Name the blood parasite species.
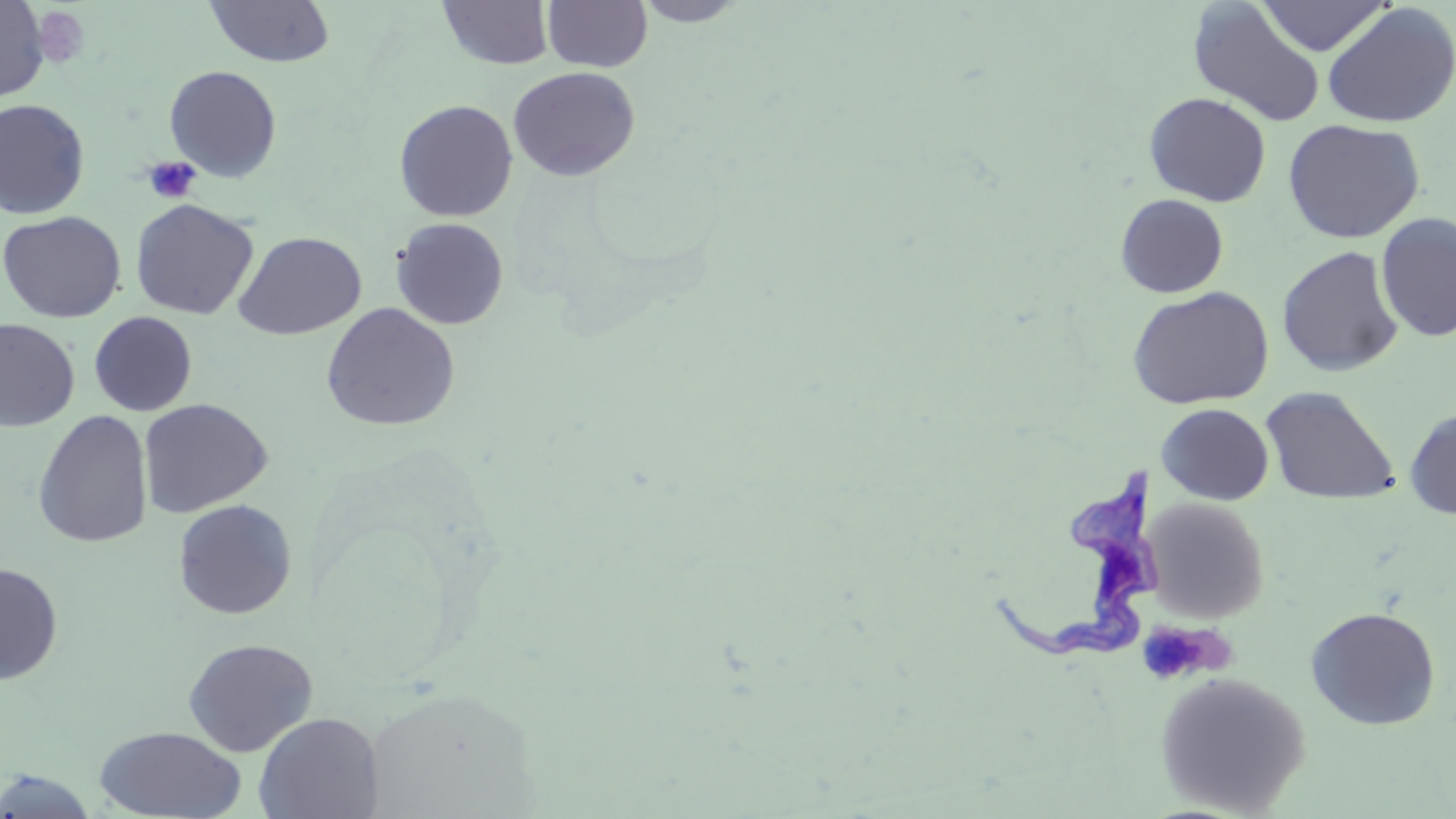
Trypanosoma brucei.

Approximate bounding boxes as [x1, y1, x2, y2] in pixels. Trypanosoma brucei locations: [985, 447, 1163, 666]. Uninfected red blood cell locations: [542, 0, 653, 72], [631, 0, 753, 27], [1255, 0, 1392, 56], [0, 1, 50, 102], [205, 1, 336, 68], [438, 1, 554, 70], [1187, 3, 1326, 128], [1321, 3, 1456, 128], [164, 65, 282, 182], [508, 66, 641, 182], [1144, 92, 1271, 207], [0, 98, 90, 219], [394, 99, 518, 222], [1282, 118, 1425, 243], [1115, 193, 1229, 298], [130, 199, 259, 320], [0, 210, 126, 323], [1376, 212, 1456, 342], [391, 217, 509, 330], [233, 231, 367, 340], [1277, 246, 1404, 377], [1126, 286, 1274, 410], [321, 302, 459, 431], [89, 311, 197, 416], [0, 319, 80, 432], [1259, 386, 1401, 506], [138, 398, 272, 518], [1156, 403, 1273, 505], [1404, 407, 1456, 520], [32, 410, 153, 548], [1143, 497, 1270, 622], [172, 499, 297, 619], [0, 562, 63, 685], [1305, 606, 1441, 730], [182, 637, 318, 757], [1154, 670, 1310, 816], [253, 712, 383, 819], [94, 726, 247, 818], [0, 769, 100, 817]. Platelet locations: [31, 5, 92, 69], [143, 156, 201, 204], [1147, 625, 1218, 677]. Image is 1456×819 pixels. Thin blood smear. May-Grünwald-Giemsa-stained preparation. Captured at 1000x magnification. One field of a larger specimen. Light microscopy.